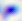

Micrograph. Captured at 400x magnification. Toxoplasma gondii is seen.